Outline each uninfected red blood cell.
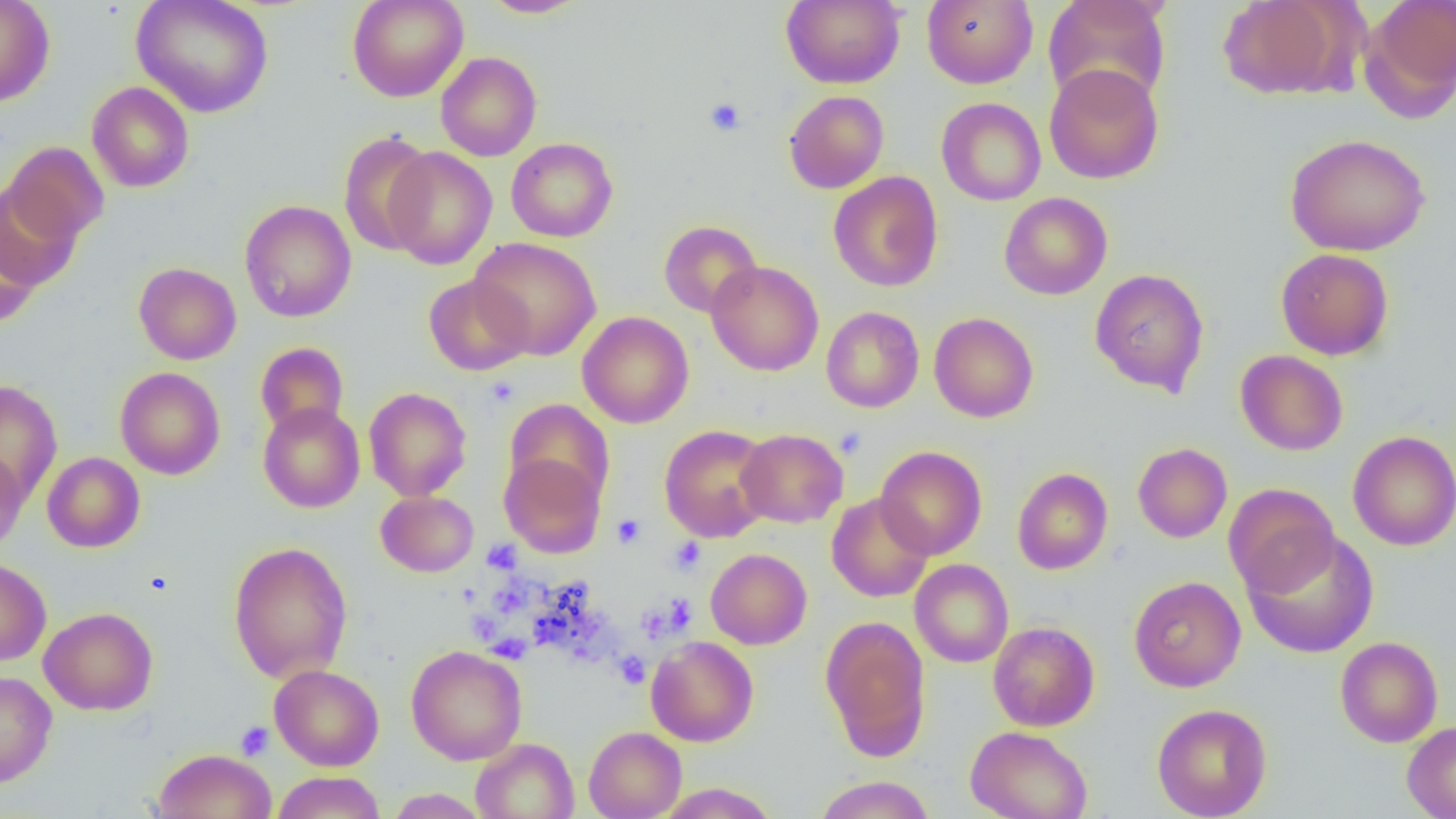
Approximate bounding boxes as named x1/y1/x2/y2 corners in pixels.
Uninfected red blood cells: (x1=0, y1=0, x2=55, y2=107), (x1=132, y1=0, x2=273, y2=118), (x1=347, y1=0, x2=468, y2=102), (x1=480, y1=0, x2=588, y2=18), (x1=781, y1=0, x2=905, y2=89), (x1=922, y1=0, x2=1038, y2=88), (x1=1043, y1=0, x2=1171, y2=107), (x1=1218, y1=0, x2=1350, y2=100), (x1=1365, y1=0, x2=1456, y2=110), (x1=436, y1=52, x2=542, y2=161), (x1=1044, y1=63, x2=1164, y2=185), (x1=87, y1=81, x2=194, y2=192), (x1=784, y1=90, x2=888, y2=193), (x1=938, y1=91, x2=1163, y2=193), (x1=936, y1=97, x2=1046, y2=206), (x1=338, y1=131, x2=437, y2=256), (x1=1284, y1=133, x2=1431, y2=256), (x1=506, y1=138, x2=618, y2=242), (x1=2, y1=142, x2=109, y2=243), (x1=384, y1=147, x2=497, y2=269), (x1=828, y1=171, x2=943, y2=292), (x1=1, y1=182, x2=80, y2=291), (x1=999, y1=192, x2=1112, y2=299), (x1=240, y1=200, x2=356, y2=322), (x1=658, y1=220, x2=762, y2=318), (x1=0, y1=223, x2=40, y2=329), (x1=470, y1=237, x2=602, y2=360), (x1=1276, y1=248, x2=1394, y2=360), (x1=707, y1=260, x2=824, y2=376), (x1=129, y1=262, x2=235, y2=476), (x1=133, y1=262, x2=241, y2=365), (x1=1090, y1=268, x2=1209, y2=396), (x1=422, y1=273, x2=532, y2=376), (x1=821, y1=306, x2=924, y2=413), (x1=577, y1=311, x2=694, y2=428), (x1=929, y1=312, x2=1039, y2=423), (x1=255, y1=342, x2=348, y2=436), (x1=1235, y1=349, x2=1348, y2=456), (x1=115, y1=367, x2=225, y2=479), (x1=0, y1=379, x2=63, y2=504), (x1=364, y1=387, x2=472, y2=500), (x1=504, y1=398, x2=615, y2=507), (x1=258, y1=402, x2=365, y2=513), (x1=659, y1=424, x2=775, y2=542), (x1=736, y1=428, x2=848, y2=527), (x1=1347, y1=430, x2=1456, y2=550), (x1=1133, y1=442, x2=1232, y2=543), (x1=875, y1=445, x2=987, y2=560), (x1=0, y1=449, x2=29, y2=559), (x1=42, y1=452, x2=145, y2=552), (x1=499, y1=452, x2=606, y2=558), (x1=1012, y1=467, x2=1113, y2=574), (x1=1224, y1=483, x2=1340, y2=598), (x1=376, y1=491, x2=478, y2=577), (x1=827, y1=494, x2=933, y2=602), (x1=1243, y1=529, x2=1380, y2=659), (x1=228, y1=540, x2=353, y2=683), (x1=706, y1=548, x2=812, y2=649), (x1=0, y1=557, x2=51, y2=666), (x1=910, y1=559, x2=1013, y2=668), (x1=1129, y1=576, x2=1245, y2=692), (x1=39, y1=607, x2=158, y2=715), (x1=820, y1=615, x2=931, y2=759), (x1=988, y1=621, x2=1100, y2=731), (x1=646, y1=635, x2=759, y2=747), (x1=1335, y1=636, x2=1443, y2=747), (x1=406, y1=645, x2=527, y2=764), (x1=269, y1=664, x2=384, y2=771), (x1=0, y1=670, x2=57, y2=788), (x1=1152, y1=702, x2=1272, y2=819), (x1=1402, y1=720, x2=1456, y2=818), (x1=584, y1=726, x2=687, y2=818), (x1=965, y1=726, x2=1092, y2=819), (x1=471, y1=738, x2=579, y2=819), (x1=153, y1=748, x2=276, y2=819), (x1=272, y1=771, x2=386, y2=819), (x1=813, y1=775, x2=936, y2=818), (x1=654, y1=782, x2=779, y2=818), (x1=385, y1=789, x2=490, y2=818).

Platelet locations: (x1=704, y1=96, x2=747, y2=137), (x1=486, y1=376, x2=520, y2=407), (x1=834, y1=425, x2=867, y2=459), (x1=612, y1=513, x2=646, y2=548), (x1=669, y1=537, x2=706, y2=575), (x1=482, y1=540, x2=522, y2=575), (x1=492, y1=589, x2=532, y2=617), (x1=657, y1=593, x2=696, y2=636), (x1=530, y1=611, x2=576, y2=656), (x1=574, y1=613, x2=611, y2=648), (x1=471, y1=619, x2=501, y2=643), (x1=488, y1=634, x2=530, y2=664), (x1=571, y1=644, x2=619, y2=666), (x1=615, y1=651, x2=650, y2=688), (x1=235, y1=722, x2=274, y2=760). Slide-level diagnosis: no evidence of blood parasites. Thin blood smear. Single field of view. Captured at 1000x magnification. Image is 1456×819 pixels. Optical microscopy.